Assess this cell for malaria.
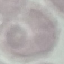
It is uninfected.

Summary:
  - Capture: smartphone through the microscope eyepiece
  - Stain: Giemsa
  - Preparation: thin blood smear
  - Image type: cell patch, automatically extracted from a larger field of view and resized to 64 × 64 pixels